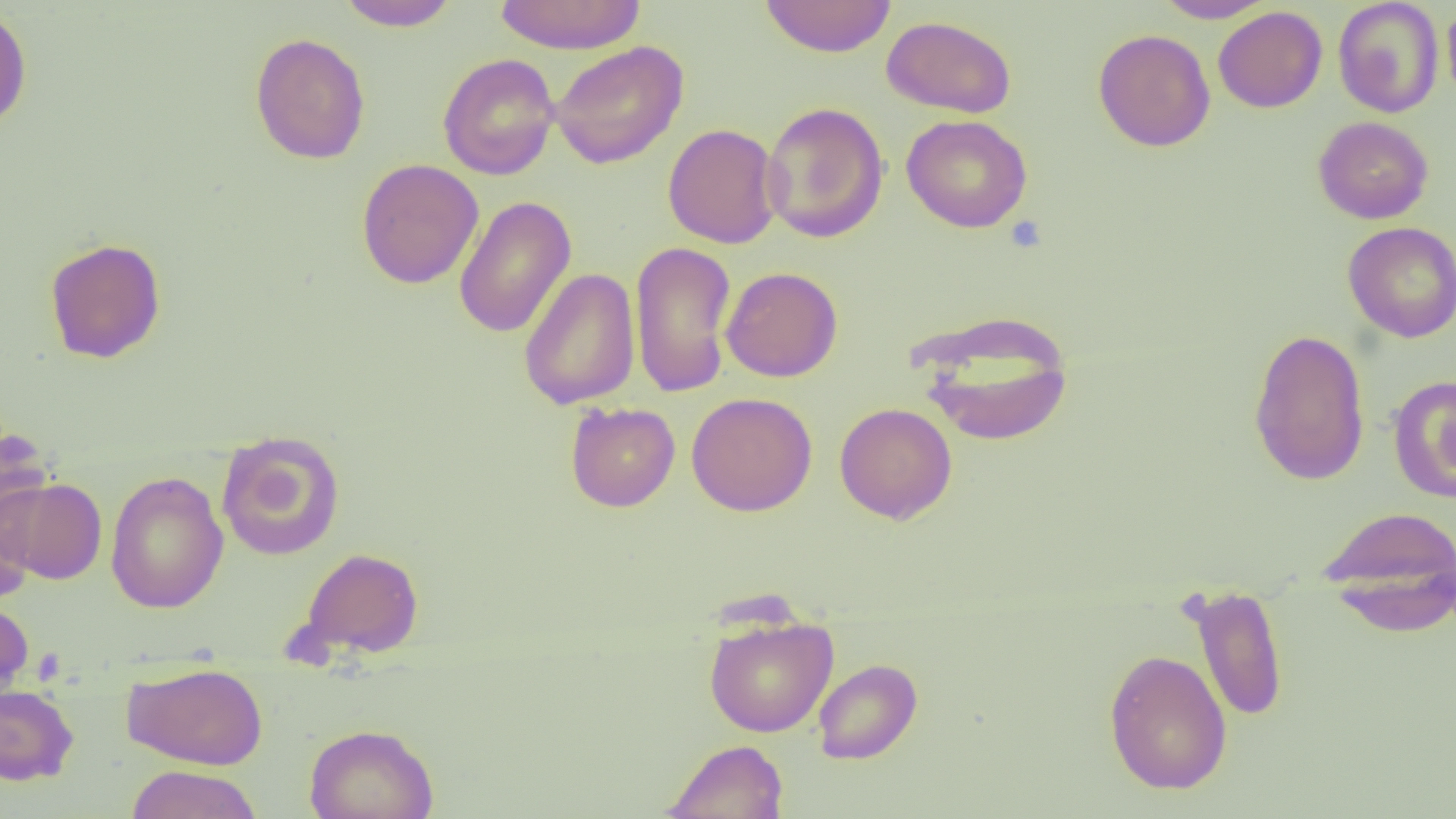

Approximate bounding boxes as (x1, y1, x2, y2) in pixels. Uninfected red blood cell locations: (335, 0, 461, 31), (492, 0, 648, 54), (759, 0, 896, 58), (1152, 0, 1276, 23), (1332, 0, 1444, 118), (1442, 3, 1456, 108), (0, 5, 32, 131), (1213, 6, 1328, 113), (881, 15, 1017, 118), (1093, 28, 1216, 152), (250, 32, 371, 165), (548, 40, 688, 169), (438, 53, 560, 180), (760, 101, 889, 243), (901, 114, 1032, 233), (1313, 116, 1434, 224), (663, 123, 782, 249), (356, 159, 484, 289), (453, 195, 576, 338), (1342, 221, 1456, 343), (44, 237, 167, 364), (630, 240, 738, 399), (721, 266, 843, 382), (519, 267, 640, 410), (917, 316, 1074, 447), (1248, 327, 1370, 486), (1387, 375, 1456, 504), (686, 392, 818, 516), (566, 402, 680, 511), (834, 402, 958, 524), (0, 427, 53, 555), (216, 430, 345, 561), (104, 470, 229, 613), (2, 477, 107, 584), (0, 493, 35, 603), (1317, 505, 1456, 619), (299, 546, 424, 658), (1188, 584, 1289, 724), (0, 595, 34, 701), (703, 615, 838, 737), (1103, 649, 1232, 795), (812, 658, 922, 764), (122, 662, 269, 769), (0, 682, 79, 786), (304, 723, 439, 819), (662, 739, 789, 819), (124, 764, 263, 819). Platelet locations: (1005, 215, 1048, 253). Slide-level diagnosis: no evidence of blood parasites. Image is 1456×819 pixels. Optical microscopy. Thin blood film. 1000x magnification. One field of a larger specimen.